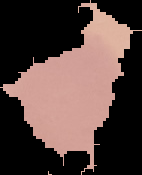
Summary:
  - Result: no Plasmodium parasites seen
  - Image type: segmented cell region with the area outside set to black
  - Image size: 142×175 pixels
  - Preparation: thin blood film